Report the malaria status of this cell.
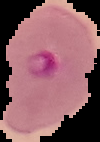
Parasitized.

{
  "image_size": "100×142 pixels",
  "preparation": "thin blood smear",
  "image_type": "segmented cell region with the area outside set to black"
}